Report the malaria status of this cell.
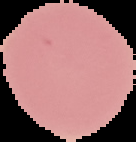
Uninfected.

Summary:
  - Preparation: thin blood film
  - Image type: segmented cell region on a black background
  - Image size: 136×142 pixels